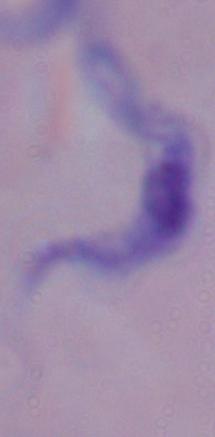

identification: trypanosome
modality: micrograph
magnification: 1000x